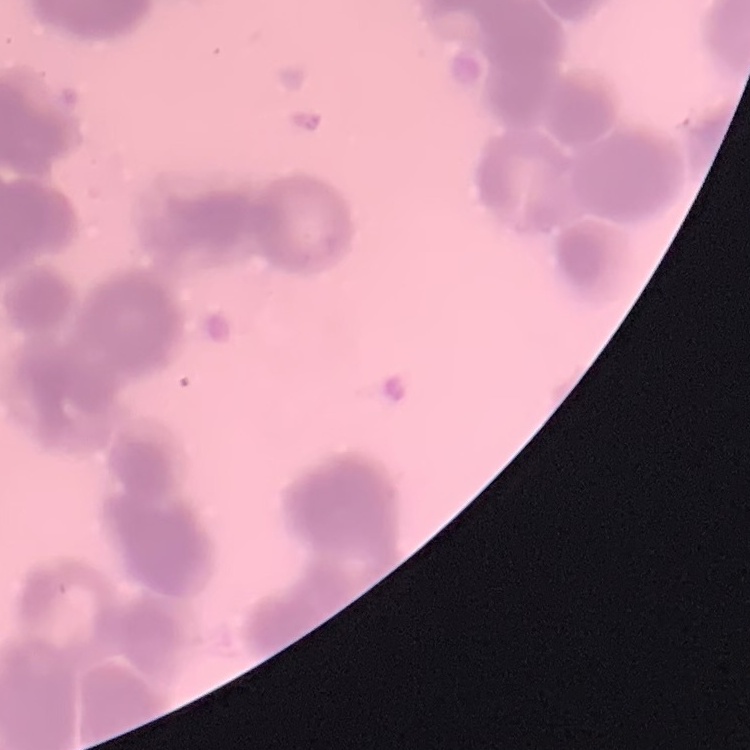

erythrocyte morphology = rouleaux formation
preparation = thin blood film
stain = Field's or Giemsa
image type = one tile cut from a larger photomicrograph